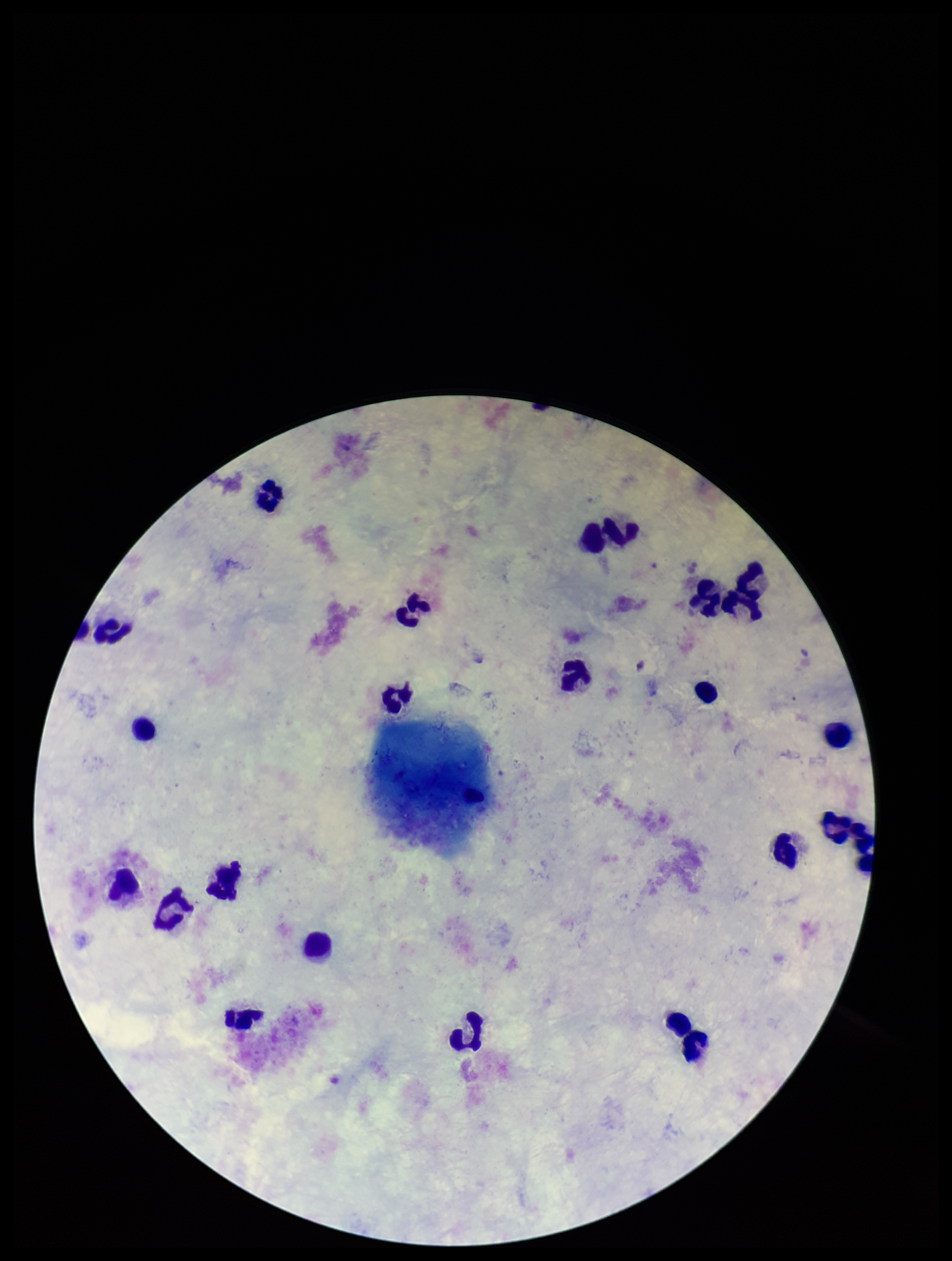
Summary:
  - Image size: 952×1261 pixels
  - Leukocyte count: 24
  - Field of view: single
  - Patient malaria status: negative
  - Capture: smartphone photograph through the microscope eyepiece
  - Plasmodium parasites: none detected
  - Stain: Giemsa
  - Parasite count: 0
  - Preparation: thick blood smear